Identify the cell.
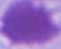
This is an erythrocyte.

modality = photomicrograph
magnification = 1000x